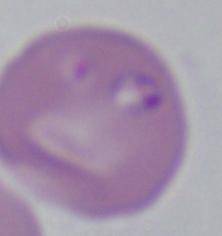 Micrograph. A Babesia parasite is shown. 1000x magnification.